Assess this cell for malaria.
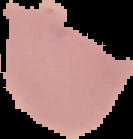

Uninfected.

Summary:
  - Image size: 133×139 pixels
  - Preparation: thin blood smear
  - Image type: segmented cell region with the area outside set to black